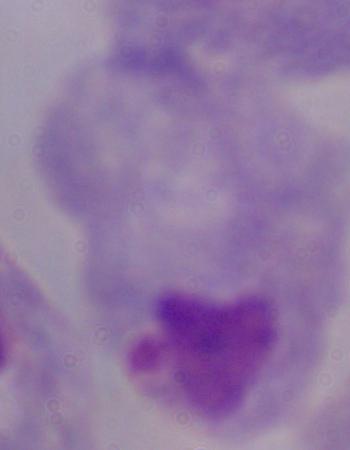
Captured at 1000x magnification. A trichomonad is seen. Photomicrograph.